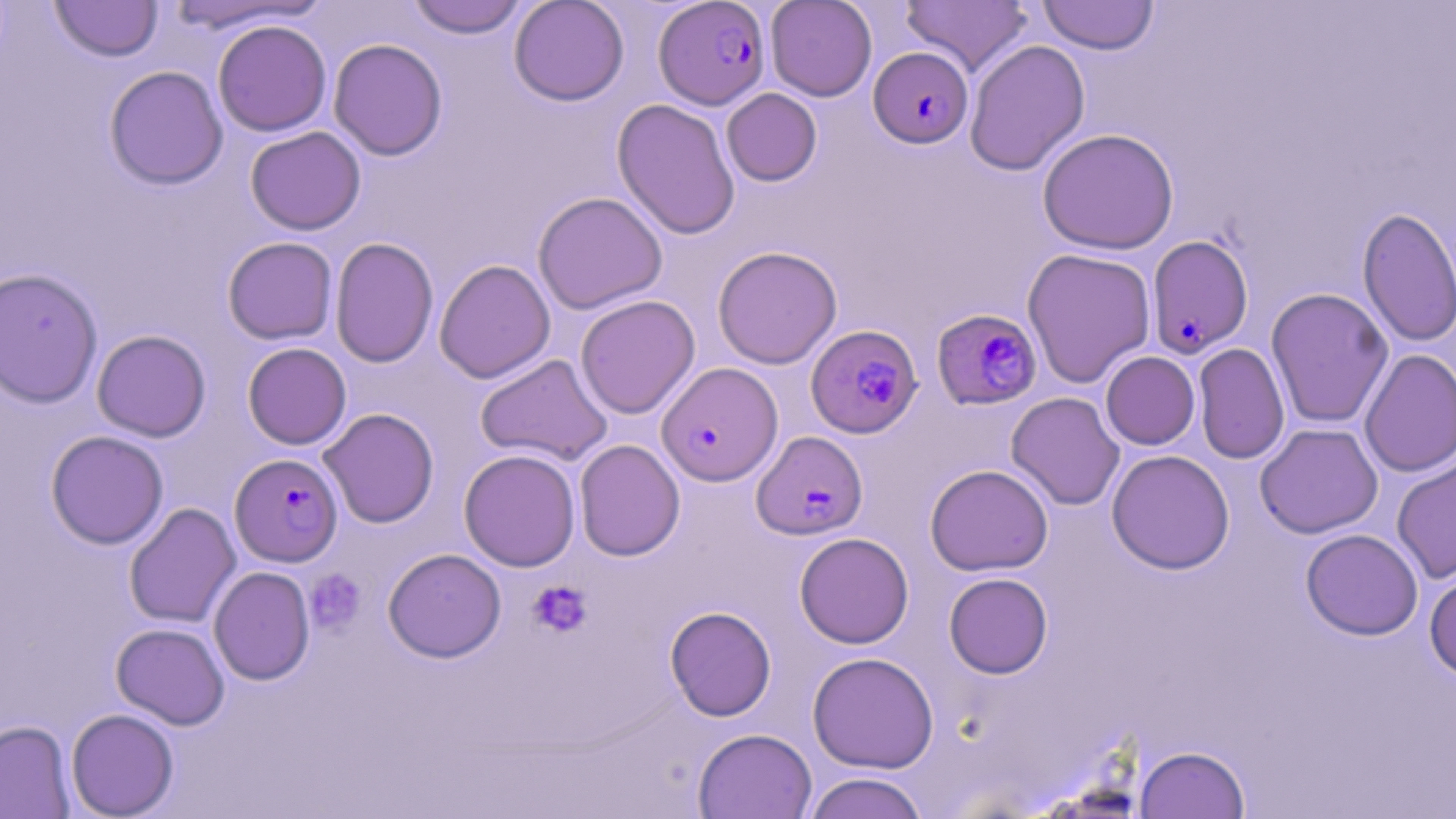
Approximate bounding boxes as named x1/y1/x2/y2 corners in pixels. Uninfected red blood cell locations: (x1=50, y1=0, x2=163, y2=62), (x1=163, y1=0, x2=328, y2=35), (x1=406, y1=0, x2=529, y2=38), (x1=509, y1=0, x2=629, y2=106), (x1=765, y1=0, x2=877, y2=101), (x1=900, y1=0, x2=1033, y2=76), (x1=1037, y1=0, x2=1159, y2=54), (x1=212, y1=20, x2=332, y2=136), (x1=328, y1=38, x2=448, y2=160), (x1=964, y1=39, x2=1090, y2=176), (x1=104, y1=65, x2=228, y2=190), (x1=721, y1=88, x2=822, y2=186), (x1=612, y1=98, x2=741, y2=240), (x1=245, y1=126, x2=366, y2=235), (x1=1037, y1=128, x2=1179, y2=254), (x1=532, y1=191, x2=668, y2=315), (x1=1357, y1=206, x2=1456, y2=347), (x1=222, y1=236, x2=338, y2=344), (x1=330, y1=237, x2=439, y2=368), (x1=712, y1=246, x2=842, y2=369), (x1=1022, y1=248, x2=1156, y2=388), (x1=434, y1=259, x2=555, y2=383), (x1=0, y1=268, x2=103, y2=408), (x1=1266, y1=288, x2=1394, y2=428), (x1=575, y1=295, x2=700, y2=419), (x1=91, y1=329, x2=211, y2=442), (x1=242, y1=342, x2=352, y2=449), (x1=1193, y1=343, x2=1289, y2=464), (x1=1359, y1=348, x2=1455, y2=478), (x1=1100, y1=351, x2=1200, y2=450), (x1=475, y1=353, x2=613, y2=466), (x1=1006, y1=392, x2=1125, y2=510), (x1=318, y1=408, x2=439, y2=528), (x1=1255, y1=423, x2=1383, y2=539), (x1=45, y1=430, x2=168, y2=549), (x1=574, y1=439, x2=685, y2=561), (x1=459, y1=449, x2=581, y2=571), (x1=1106, y1=449, x2=1235, y2=574), (x1=1392, y1=455, x2=1456, y2=583), (x1=925, y1=464, x2=1054, y2=576), (x1=124, y1=502, x2=241, y2=628), (x1=1300, y1=529, x2=1423, y2=640), (x1=794, y1=532, x2=913, y2=648), (x1=383, y1=548, x2=506, y2=663), (x1=208, y1=566, x2=315, y2=685), (x1=1424, y1=568, x2=1456, y2=682), (x1=944, y1=572, x2=1053, y2=678), (x1=665, y1=606, x2=776, y2=721), (x1=111, y1=622, x2=230, y2=729), (x1=807, y1=651, x2=939, y2=773), (x1=66, y1=708, x2=179, y2=818), (x1=0, y1=720, x2=74, y2=818), (x1=693, y1=728, x2=816, y2=818), (x1=1136, y1=745, x2=1249, y2=819), (x1=803, y1=772, x2=929, y2=819). Plasmodium falciparum-infected red blood cell locations: (x1=654, y1=1, x2=771, y2=109), (x1=869, y1=47, x2=973, y2=148), (x1=1146, y1=235, x2=1254, y2=358), (x1=933, y1=308, x2=1044, y2=410), (x1=808, y1=323, x2=924, y2=438), (x1=656, y1=361, x2=783, y2=486), (x1=752, y1=431, x2=868, y2=540), (x1=230, y1=453, x2=342, y2=567). Platelet locations: (x1=305, y1=569, x2=365, y2=634), (x1=527, y1=580, x2=593, y2=638). Slide-level diagnosis: Plasmodium falciparum. 1000x magnification. Light microscopy. May-Grünwald-Giemsa stain. One field of a larger specimen. Thin blood film. Image is 1456×819 pixels.